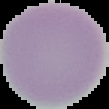

Summary:
  - Result: negative for Plasmodium parasites
  - Image size: 109×109 pixels
  - Preparation: thin blood film
  - Image type: segmented cell region on a black background